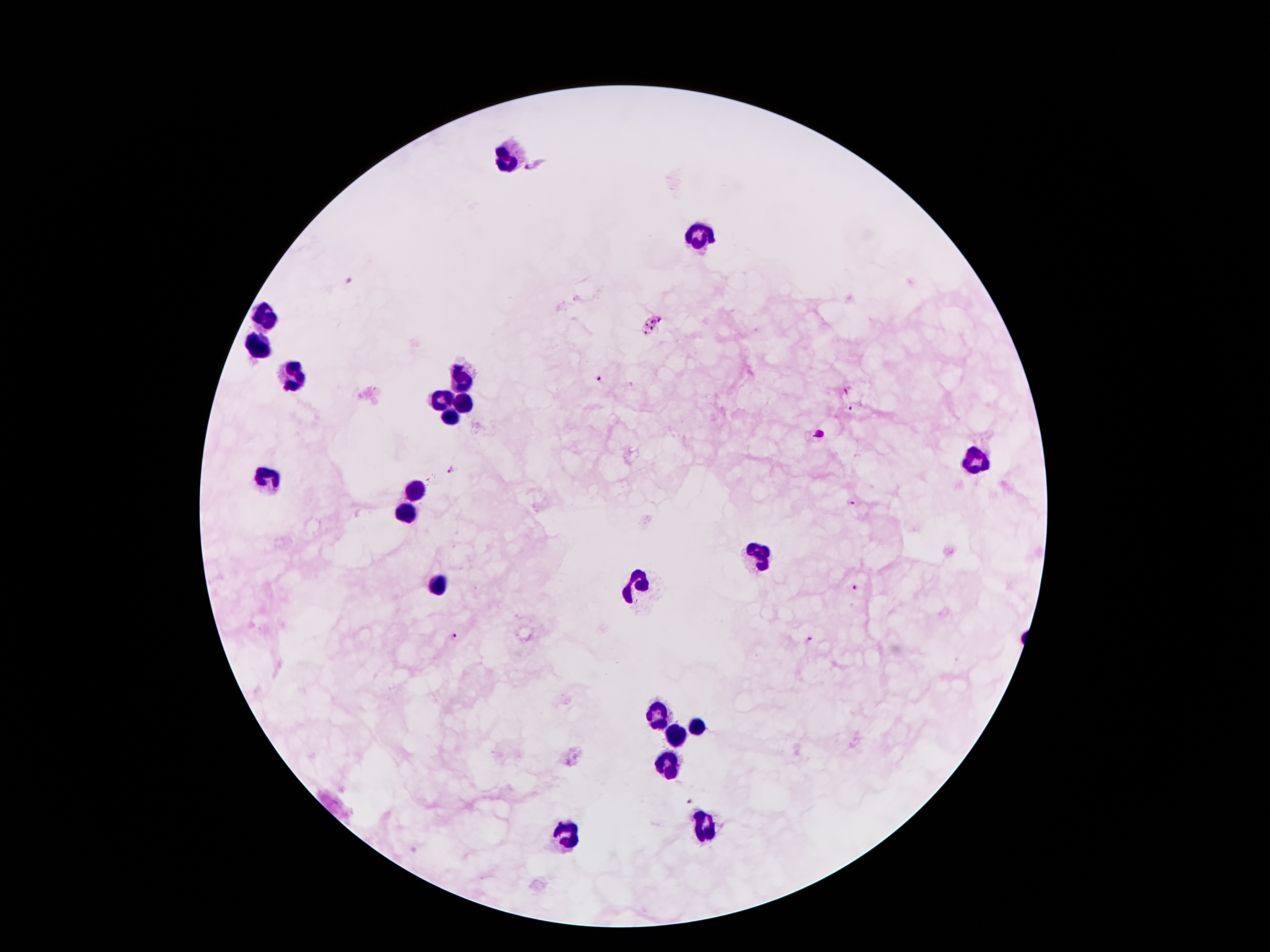

Approximate centers as [x, y] in pixels. Leukocyte locations: [511, 153], [697, 237], [268, 317], [257, 348], [293, 375], [457, 378], [441, 401], [466, 401], [449, 414], [969, 460], [266, 478], [413, 492], [407, 512], [758, 553], [438, 585], [638, 585], [658, 716], [697, 726], [674, 735], [667, 767], [706, 825], [565, 835]. Plasmodium parasite locations: [535, 163], [349, 280], [654, 324], [598, 377], [846, 392], [850, 408], [450, 470], [850, 502], [855, 589], [452, 639], [811, 641], [688, 799]. Single field of view. Image is 1270×952 pixels. Patient malaria status: infected with Plasmodium falciparum. Smartphone photograph taken through the microscope eyepiece. 100x magnification. Thick blood film. Giemsa stain.